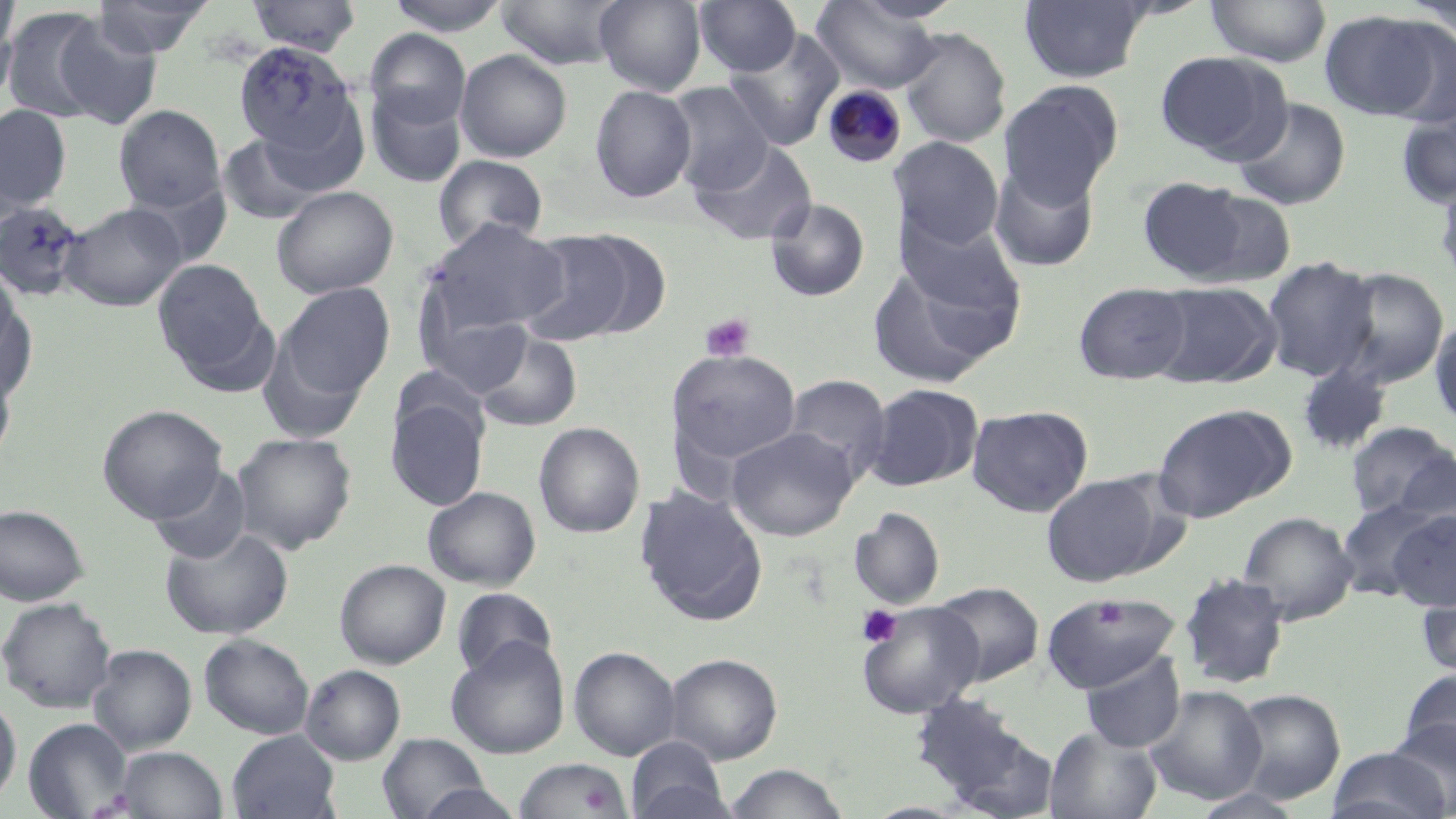 Approximate bounding boxes as [x1, y1, x2, y2] in pixels. Platelet locations: [701, 312, 754, 362], [1095, 597, 1128, 630], [858, 604, 904, 648]. Uninfected red blood cell locations: [0, 0, 20, 88], [92, 0, 214, 57], [247, 0, 361, 55], [385, 0, 512, 36], [496, 0, 630, 70], [594, 0, 706, 95], [695, 0, 801, 76], [1205, 0, 1331, 67], [812, 1, 944, 93], [1019, 1, 1151, 83], [1399, 1, 1455, 41], [1, 6, 112, 124], [1318, 10, 1453, 123], [53, 17, 164, 130], [899, 27, 1012, 148], [365, 28, 470, 130], [723, 30, 844, 150], [233, 41, 361, 164], [455, 49, 573, 162], [1155, 51, 1288, 162], [998, 81, 1123, 205], [664, 82, 774, 195], [589, 84, 696, 203], [366, 87, 467, 188], [1231, 98, 1351, 210], [114, 104, 225, 214], [1, 105, 72, 210], [1395, 105, 1456, 210], [218, 132, 325, 225], [891, 136, 1003, 249], [691, 139, 817, 246], [433, 155, 548, 252], [989, 162, 1100, 272], [1434, 175, 1456, 293], [1137, 176, 1256, 283], [127, 179, 233, 269], [271, 185, 398, 299], [765, 198, 870, 302], [0, 201, 86, 301], [58, 202, 186, 311], [896, 213, 1023, 318], [426, 220, 570, 336], [515, 228, 654, 346], [1262, 256, 1378, 382], [153, 259, 269, 376], [0, 260, 21, 363], [866, 265, 1006, 388], [1328, 267, 1450, 389], [0, 273, 33, 394], [1149, 281, 1280, 388], [1074, 282, 1191, 384], [278, 284, 395, 401], [417, 296, 534, 399], [1430, 316, 1456, 431], [256, 329, 371, 445], [473, 330, 583, 432], [667, 349, 802, 466], [0, 361, 17, 471], [1296, 361, 1392, 456], [782, 374, 891, 484], [863, 383, 984, 491], [385, 398, 489, 511], [97, 403, 227, 524], [1151, 403, 1295, 523], [968, 405, 1093, 517], [1345, 421, 1454, 519], [533, 422, 646, 538], [727, 427, 858, 541], [231, 432, 357, 554], [1388, 448, 1456, 549], [148, 464, 253, 563], [1042, 474, 1164, 586], [423, 486, 541, 591], [634, 486, 768, 626], [1334, 497, 1450, 601], [0, 504, 90, 606], [849, 507, 945, 610], [1387, 509, 1456, 612], [1238, 511, 1358, 625], [161, 525, 294, 640], [335, 559, 451, 670], [1179, 571, 1290, 689], [1416, 578, 1456, 680], [932, 581, 1044, 686], [452, 587, 556, 680], [1047, 593, 1178, 693], [0, 597, 116, 713], [858, 601, 983, 718], [199, 634, 314, 739], [446, 636, 569, 759], [88, 644, 197, 755], [569, 646, 680, 760], [665, 652, 782, 763], [1080, 652, 1186, 753], [300, 663, 405, 765], [1399, 668, 1456, 768], [1145, 686, 1267, 804], [1228, 688, 1346, 806], [909, 692, 1052, 814], [0, 693, 21, 808], [23, 717, 133, 818], [1387, 719, 1456, 818], [1044, 725, 1162, 819], [228, 730, 342, 819], [377, 733, 491, 818], [627, 736, 732, 819], [1325, 745, 1454, 818], [116, 746, 228, 819], [514, 757, 631, 819], [724, 763, 850, 819], [415, 783, 525, 819]. Plasmodium malariae-infected red blood cell locations: [821, 84, 907, 168]. Slide-level diagnosis: Plasmodium malariae. Light microscopy. Thin blood smear. Single field of view. Image is 1456×819 pixels. May-Grünwald-Giemsa-stained preparation. Captured at 1000x magnification.